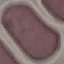
Summary:
  - Malaria status: uninfected
  - Stain: Giemsa
  - Preparation: thin smear
  - Capture: smartphone through the microscope eyepiece
  - Image type: cell patch, automatically extracted from a larger field of view and resized to 64 × 64 pixels